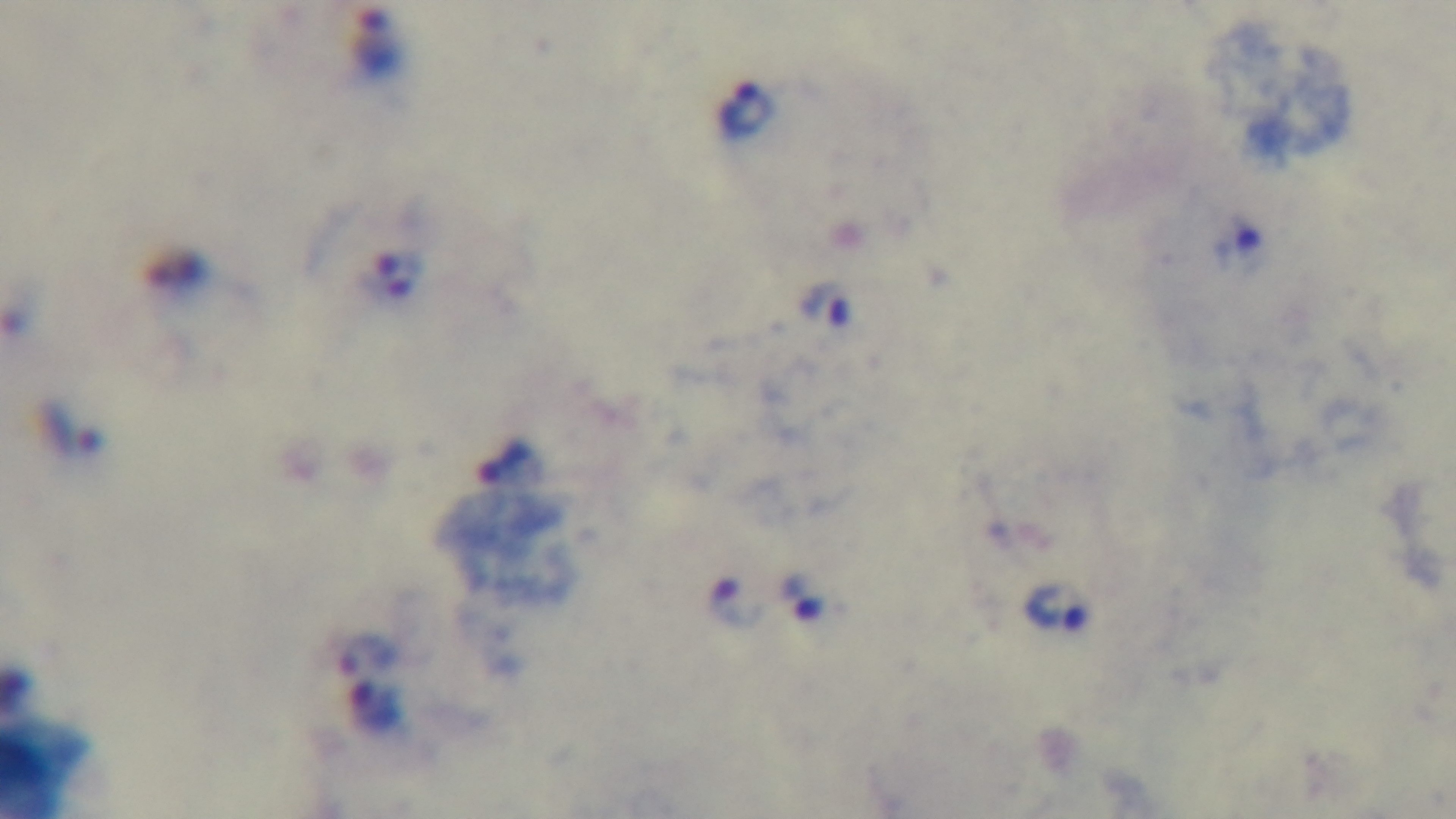

Photomicrograph. Oil-immersion objective, 100x. Mounted 4K digital camera. Preparation: thick blood film. One field from the slide. Giemsa-stained. Malaria status: positive.